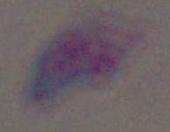
modality = photomicrograph
identification = Toxoplasma gondii
magnification = 1000x